State which parasite is depicted.
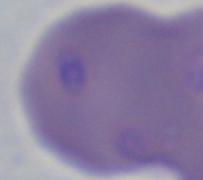

This is Babesia.

Micrograph. Captured at 1000x magnification.